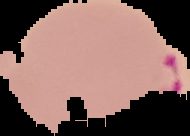
Summary:
  - Image type: segmented cell region with the area outside set to black
  - Preparation: thin blood film
  - Result: malaria parasites detected
  - Image size: 190×136 pixels